Assess this cell for malaria.
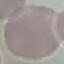
It is uninfected.

Photographed with a smartphone camera at the microscope eyepiece. Thin blood film. Giemsa stain. Cell patch, automatically extracted from a larger field of view and resized to 64 × 64 pixels.